Assess this cell for malaria.
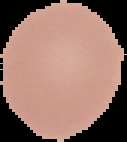

Uninfected.

preparation: thin blood smear
image_size: 127×142 pixels
image_type: segmented cell region with the area outside set to black